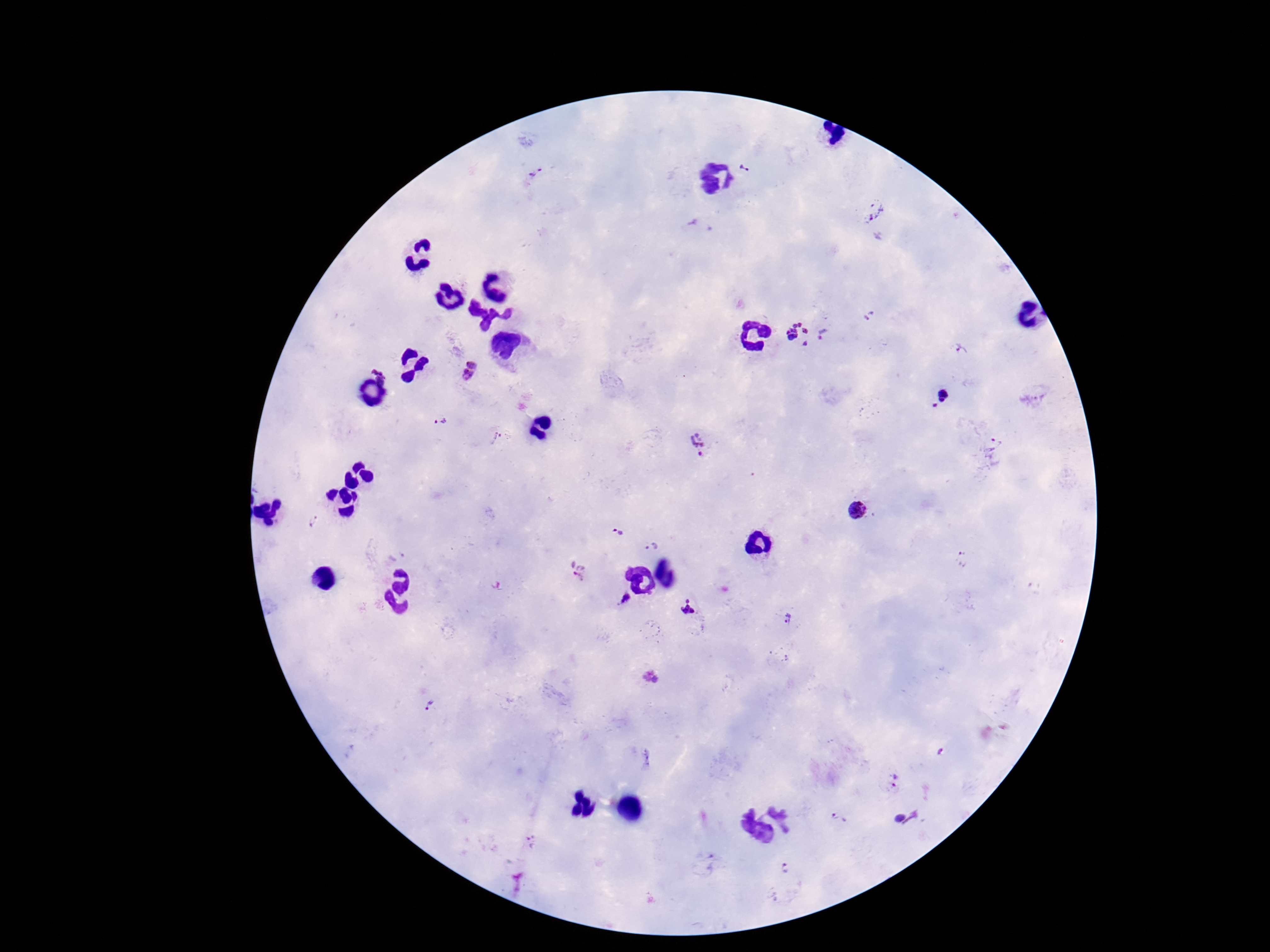

Approximate centers as [x, y] in pixels.
Summary:
  - Plasmodium parasite locations: [746, 167], [536, 173], [876, 211], [701, 228], [805, 335], [961, 350], [469, 373], [939, 398], [440, 423], [497, 437], [698, 443], [994, 455], [857, 511], [312, 521], [617, 533], [652, 547], [577, 573], [626, 600], [688, 608], [786, 619], [649, 678], [428, 706], [896, 779], [907, 818], [839, 819], [532, 843], [785, 868]
  - Stain: Giemsa
  - Preparation: thick peripheral-blood smear
  - Field of view: one from this slide
  - Capture: smartphone camera through the microscope eyepiece
  - Patient malaria status: positive
  - Image size: 1270×952 pixels
  - Magnification: 100x